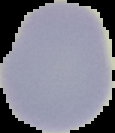

image_size: 115×133 pixels
preparation: thin blood smear
image_type: segmented cell region with the area outside set to black
result: negative for malaria parasites